Give the extent of all Plasmodium falciparum-infected red blood cells.
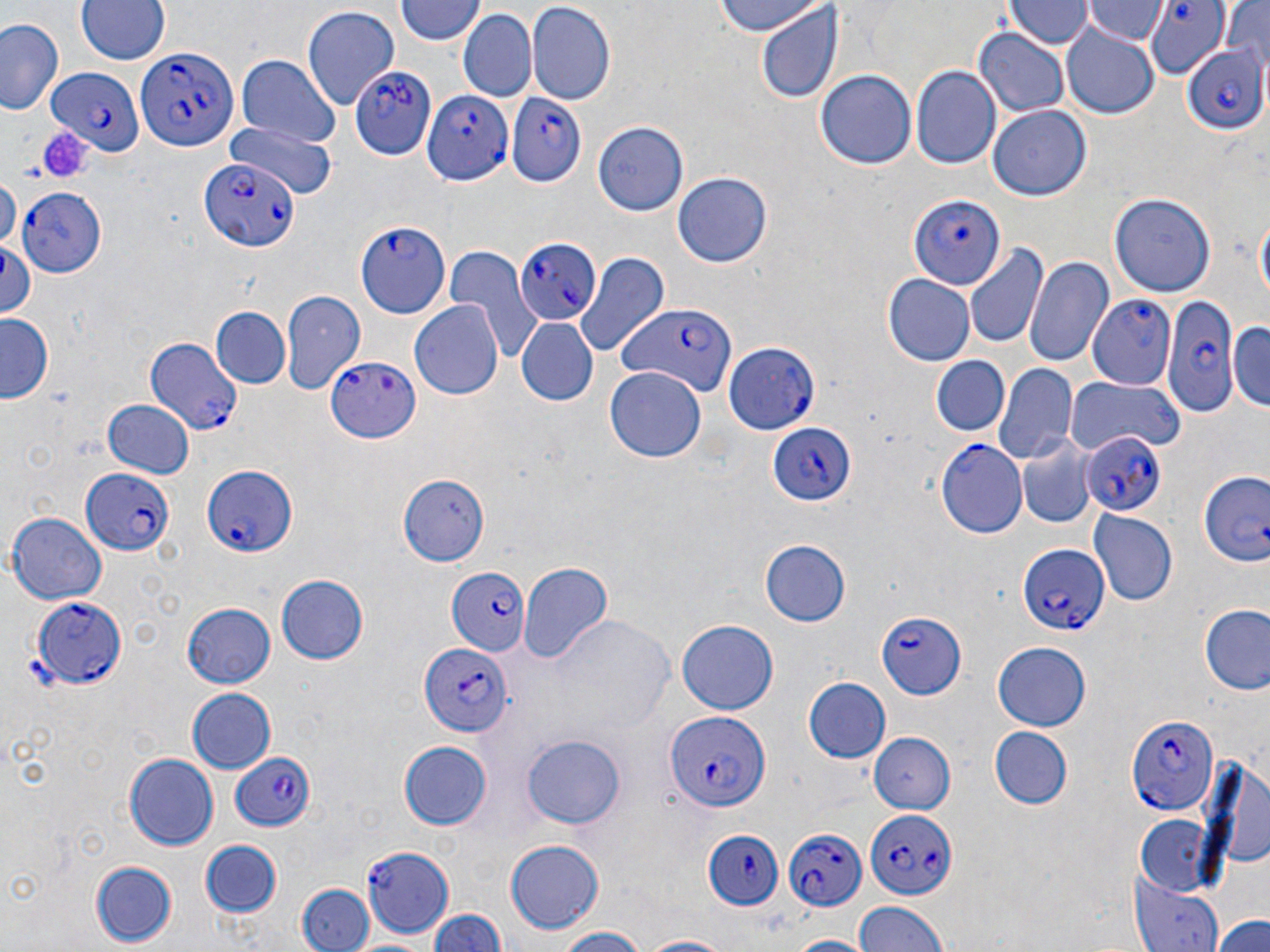
Approximate bounding boxes as [x1, y1, x2, y2] in pixels.
Plasmodium falciparum-infected red blood cells: [1143, 2, 1228, 75], [1181, 41, 1268, 134], [133, 46, 238, 149], [354, 59, 439, 165], [50, 66, 144, 153], [505, 89, 588, 189], [422, 91, 512, 185], [198, 159, 297, 253], [15, 187, 106, 278], [908, 192, 1006, 293], [355, 222, 449, 318], [515, 237, 602, 324], [1161, 292, 1239, 417], [1088, 293, 1177, 391], [618, 300, 738, 396], [142, 335, 243, 436], [723, 341, 819, 435], [326, 355, 422, 442], [767, 422, 856, 508], [1082, 431, 1167, 514], [936, 439, 1027, 540], [200, 465, 295, 559], [81, 469, 175, 556], [1200, 471, 1269, 567], [1016, 542, 1109, 636], [448, 567, 530, 657], [30, 598, 127, 688], [877, 608, 968, 698], [419, 643, 513, 738], [1124, 710, 1218, 815], [667, 711, 774, 811], [230, 752, 318, 832], [865, 808, 956, 900], [782, 827, 867, 912], [702, 830, 784, 910], [361, 842, 454, 936].

Summary:
  - Uninfected red blood cell locations: [76, 0, 171, 65], [713, 0, 824, 38], [1221, 0, 1269, 78], [395, 1, 486, 47], [1005, 2, 1089, 50], [527, 3, 617, 105], [1085, 3, 1167, 47], [756, 4, 844, 105], [301, 6, 399, 110], [458, 11, 536, 105], [0, 16, 63, 118], [1059, 26, 1161, 118], [974, 28, 1071, 119], [238, 55, 340, 149], [912, 67, 1001, 171], [815, 68, 916, 169], [988, 105, 1092, 201], [223, 119, 335, 202], [592, 120, 689, 217], [673, 169, 772, 266], [0, 174, 19, 254], [1111, 192, 1215, 297], [1255, 204, 1269, 317], [0, 236, 37, 324], [964, 244, 1050, 352], [446, 246, 540, 361], [573, 251, 669, 360], [1024, 255, 1113, 371], [883, 275, 974, 366], [281, 291, 366, 391], [409, 298, 503, 400], [210, 307, 290, 390], [0, 315, 52, 403], [516, 318, 597, 405], [1229, 321, 1270, 412], [931, 355, 1008, 437], [995, 362, 1077, 465], [605, 367, 707, 463], [1067, 373, 1185, 455], [102, 397, 195, 478], [1015, 440, 1097, 530], [398, 474, 491, 565], [1090, 510, 1178, 605], [6, 512, 106, 606], [758, 540, 849, 627], [518, 561, 614, 670], [275, 573, 369, 665], [181, 602, 276, 689], [1200, 602, 1270, 696], [675, 618, 780, 717], [990, 642, 1092, 730], [804, 677, 890, 764], [185, 687, 275, 774], [989, 727, 1072, 809], [521, 731, 627, 829], [866, 731, 955, 814], [399, 739, 495, 830], [123, 752, 217, 851], [1196, 752, 1270, 878], [1133, 814, 1218, 893], [503, 839, 607, 934], [200, 841, 282, 917], [88, 860, 179, 947], [1130, 871, 1224, 952], [297, 885, 373, 952], [851, 900, 946, 951], [429, 907, 508, 952], [1214, 911, 1270, 952], [550, 926, 649, 952], [787, 934, 868, 952], [348, 935, 443, 952], [635, 935, 742, 952]
  - Platelet locations: [36, 123, 94, 184]
  - Slide-level diagnosis: Plasmodium falciparum
  - Magnification: 1000x
  - Preparation: thin blood film
  - Modality: optical microscopy
  - Field of view: single
  - Image size: 1270×952 pixels
  - Stain: May-Grünwald-Giemsa